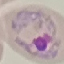
Result: malaria parasites identified. Automatically extracted cell patch, resized to 64 × 64 pixels. Thin smear of blood. Acquired by smartphone through the microscope eyepiece. Giemsa stain.